Assess this cell for malaria.
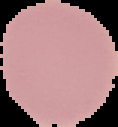
Uninfected.

Image is 118×127 pixels. From a thin blood smear. Cell region segmented out of the field of view; the surrounding area is masked to black.